Name the blood parasite species.
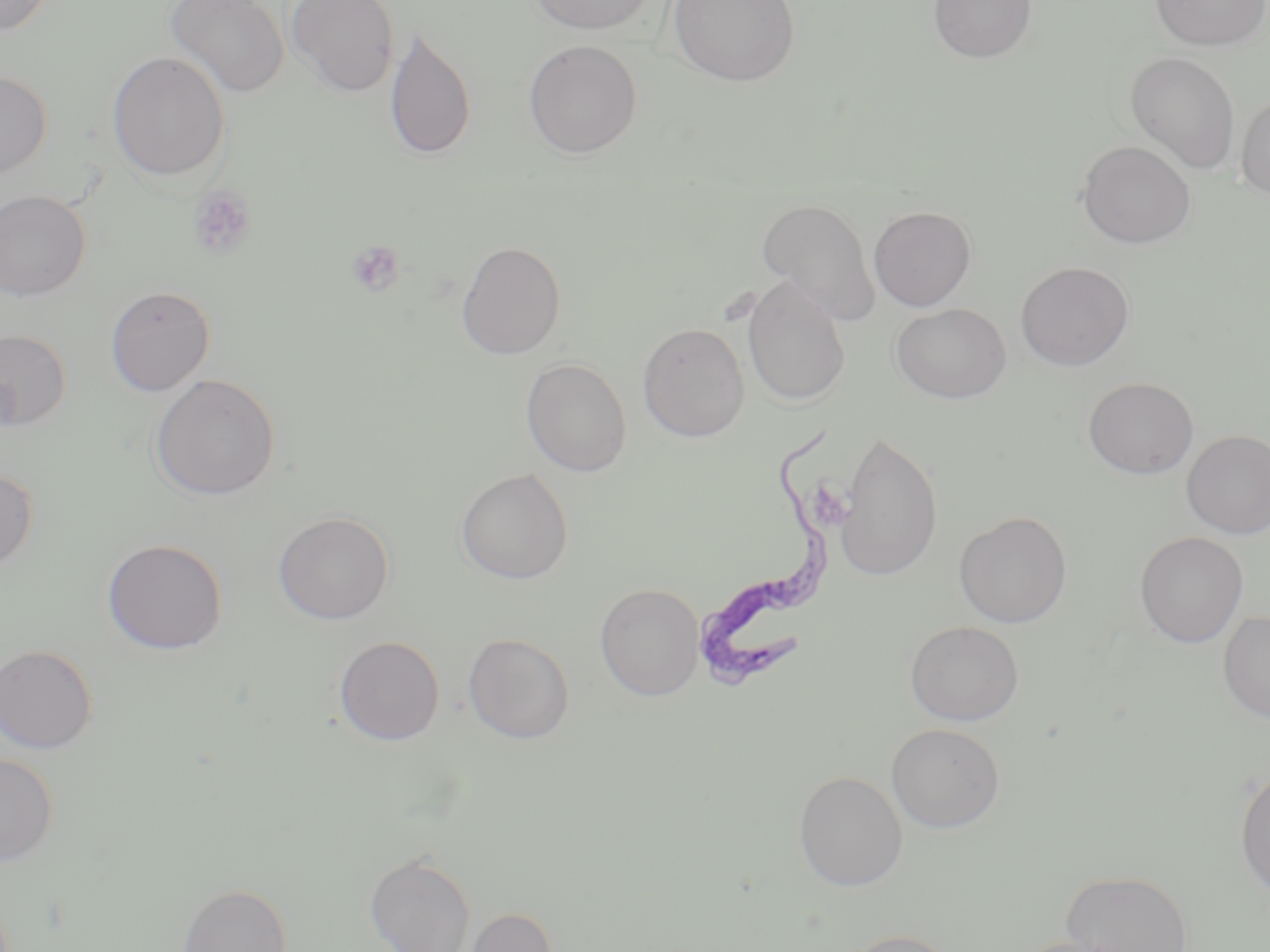

Trypanosoma brucei.

Approximate bounding boxes as [x1, y1, x2, y2] in pixels. Platelet locations: [188, 184, 257, 261], [346, 240, 405, 297]. Uninfected red blood cell locations: [0, 0, 55, 37], [165, 0, 290, 99], [286, 0, 399, 97], [525, 0, 659, 35], [667, 0, 800, 87], [928, 0, 1038, 64], [1149, 0, 1270, 51], [385, 27, 476, 162], [523, 40, 643, 158], [107, 51, 231, 183], [1125, 51, 1240, 174], [0, 71, 52, 179], [1236, 91, 1270, 200], [1077, 140, 1195, 248], [0, 190, 91, 301], [756, 197, 881, 324], [868, 205, 976, 311], [456, 240, 566, 360], [1015, 261, 1134, 371], [741, 276, 852, 407], [105, 285, 215, 396], [891, 303, 1011, 403], [637, 322, 750, 442], [0, 329, 72, 431], [521, 358, 632, 477], [151, 374, 280, 502], [1083, 377, 1199, 479], [1182, 429, 1270, 539], [836, 432, 942, 582], [0, 468, 38, 572], [455, 468, 573, 584], [273, 511, 395, 624], [954, 511, 1072, 628], [1134, 531, 1248, 647], [101, 537, 229, 655], [595, 583, 705, 701], [1217, 609, 1270, 723], [905, 620, 1024, 725], [463, 633, 574, 743], [334, 635, 445, 746], [0, 644, 98, 754], [886, 723, 1006, 833], [0, 755, 58, 866], [1234, 765, 1270, 898], [793, 770, 908, 890], [364, 852, 476, 952], [1060, 869, 1193, 952], [176, 883, 291, 952], [459, 905, 558, 952], [834, 929, 962, 952], [1011, 936, 1131, 952]. Trypanosoma brucei locations: [696, 422, 832, 700]. Captured at 1000x magnification. May-Grünwald-Giemsa stain. One field of a larger specimen. Thin blood smear. Image is 1270×952 pixels. Optical microscopy.